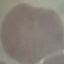

Summary:
  - Result: no malaria parasites seen
  - Stain: Giemsa
  - Capture: smartphone camera at the microscope eyepiece
  - Preparation: thin blood film
  - Image type: automatically extracted cell patch, resized to 64 × 64 pixels